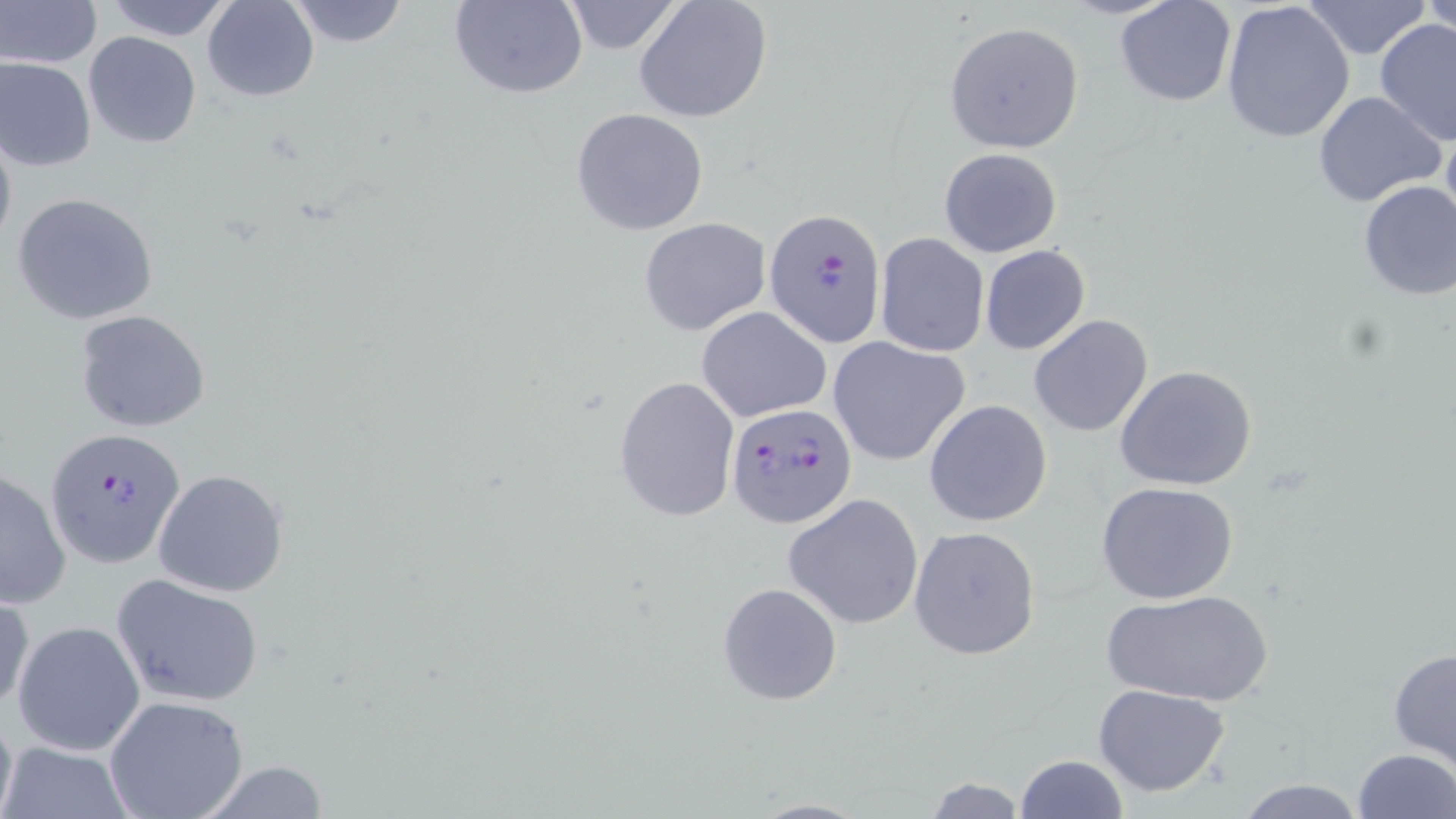

Summary:
  - Coordinate format: approximate bounding boxes as [x1, y1, x2, y2] in pixels
  - Uninfected red blood cell locations: [0, 0, 100, 69], [102, 0, 233, 41], [204, 0, 319, 101], [284, 0, 410, 48], [450, 0, 589, 99], [559, 0, 688, 55], [1221, 0, 1354, 144], [1300, 0, 1434, 59], [1422, 0, 1456, 36], [632, 1, 773, 124], [1115, 1, 1236, 107], [1375, 18, 1456, 148], [943, 22, 1084, 154], [83, 32, 200, 148], [0, 57, 97, 172], [1312, 91, 1447, 209], [571, 108, 709, 235], [1440, 110, 1456, 244], [0, 124, 16, 255], [939, 147, 1062, 258], [1356, 180, 1456, 303], [12, 192, 159, 326], [639, 217, 770, 336], [874, 233, 989, 357], [980, 246, 1090, 354], [697, 306, 834, 423], [73, 308, 211, 433], [1028, 313, 1153, 437], [829, 336, 970, 467], [1114, 364, 1258, 491], [614, 375, 740, 523], [924, 400, 1053, 526], [1, 468, 72, 609], [153, 468, 289, 597], [1096, 481, 1240, 605], [783, 493, 923, 629], [908, 525, 1042, 660], [111, 572, 265, 708], [718, 582, 842, 706], [1101, 588, 1273, 707], [0, 589, 34, 717], [12, 620, 146, 757], [1387, 646, 1456, 772], [1093, 683, 1232, 797], [103, 695, 249, 819], [0, 698, 18, 819], [1, 741, 134, 819], [1350, 748, 1454, 819], [1013, 753, 1127, 819], [189, 762, 329, 819], [919, 775, 1032, 817], [1232, 776, 1367, 817], [746, 798, 875, 818]
  - Plasmodium falciparum-infected red blood cell locations: [764, 209, 885, 346], [724, 403, 856, 529], [45, 430, 187, 568]
  - Slide-level diagnosis: Plasmodium falciparum
  - Field of view: one of a larger specimen
  - Image size: 1456×819 pixels
  - Stain: May-Grünwald-Giemsa
  - Preparation: thin blood film
  - Modality: light microscopy
  - Magnification: 1000x